Assess this cell for malaria.
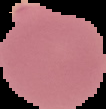

Uninfected.

preparation = thin blood film
image size = 106×109 pixels
image type = segmented cell region on a black background